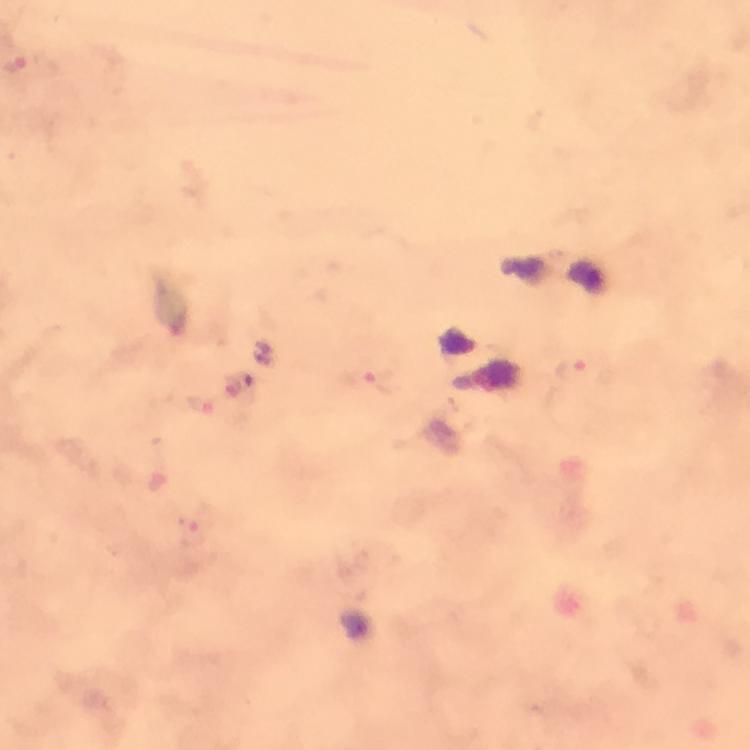
{
  "malaria_parasite_locations": "approximate centers as (x, y) in pixels: (574, 371), (381, 383), (233, 384)",
  "context": "from a malaria diagnostic workup",
  "magnification": "100x",
  "capture": "smartphone photograph through a microscope",
  "immersion_oil": "applied",
  "stain": "Giemsa",
  "preparation": "thick smear",
  "cropped_from": "a single field of view",
  "image_size": "750×750 pixels"
}